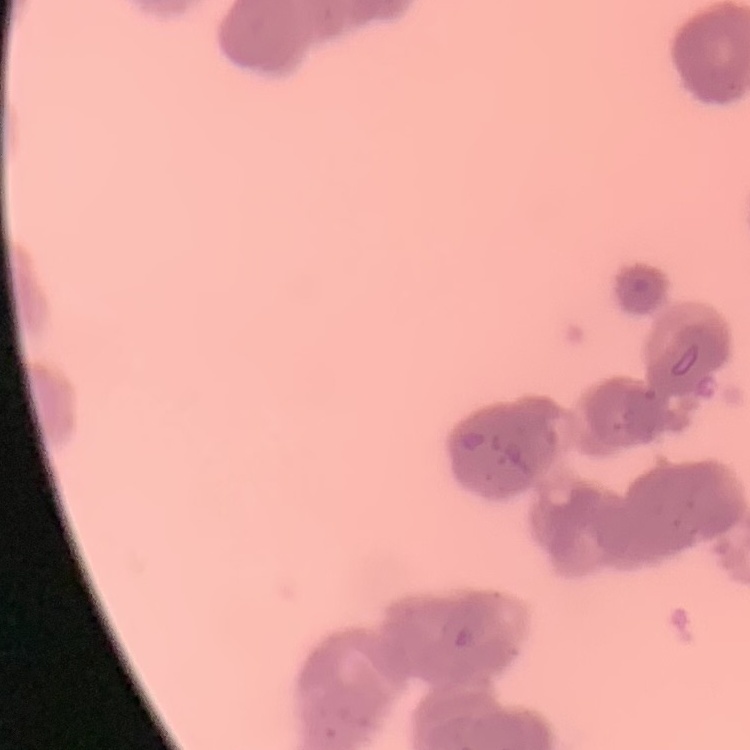
red_blood_cell_morphology: rouleaux formation
stain: Field's or Giemsa
preparation: thin blood smear
image_type: square crop of a larger photomicrograph